Evaluate for Plasmodium parasites.
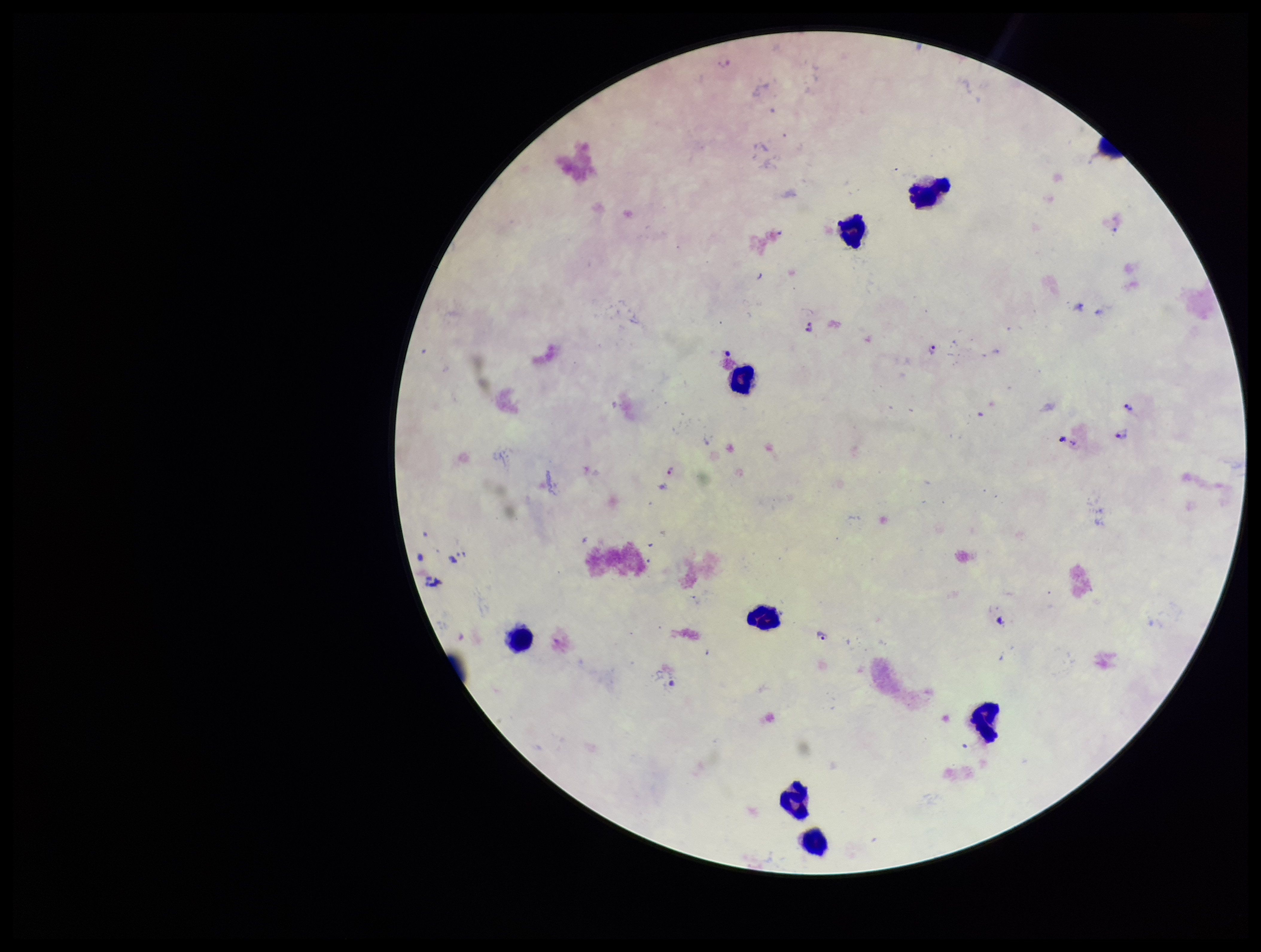
Identified.

Giemsa stain. Smartphone photograph taken through the eyepiece of a microscope. Species reported for this patient: Plasmodium falciparum. Leukocyte count: 9. Preparation: thick blood smear. Parasite count: 8. Patient malaria status: infected. One field from this slide. Image is 1261×952 pixels.